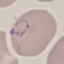

malaria status = parasitized
stain = Giemsa
image type = automatically extracted cell patch, resized to 64 × 64 pixels
capture = smartphone through the microscope eyepiece
preparation = thin blood smear